Report the malaria status of this cell.
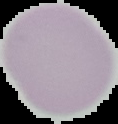

It is uninfected.

Summary:
  - Preparation: thin blood film
  - Image type: cell region segmented out of the field of view; surrounding area masked to black
  - Image size: 118×124 pixels